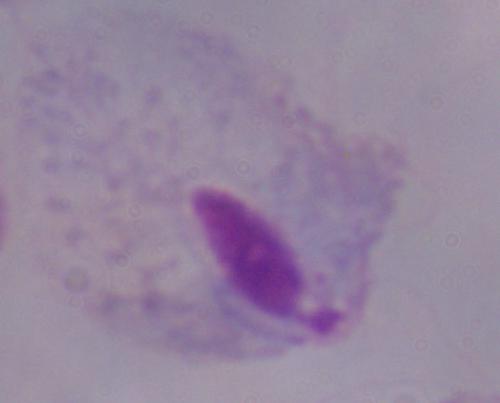
identification = trichomonad
modality = micrograph
magnification = 1000x